Describe the morphology of the red blood cells.
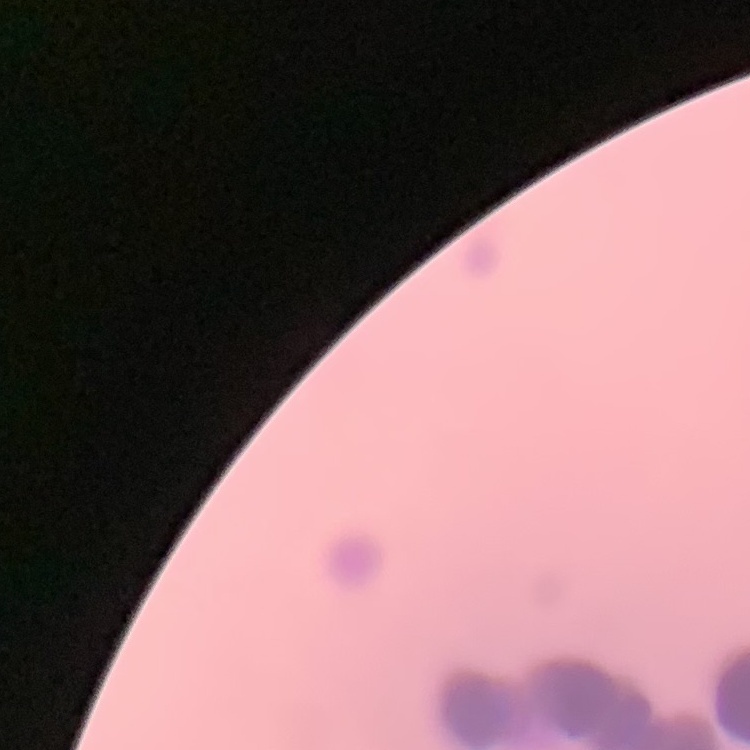
They show rouleaux formation.

Summary:
  - Stain: Field's or Giemsa
  - Image type: square crop of a larger photomicrograph
  - Preparation: thin blood film